Comment on the morphology of the erythrocytes.
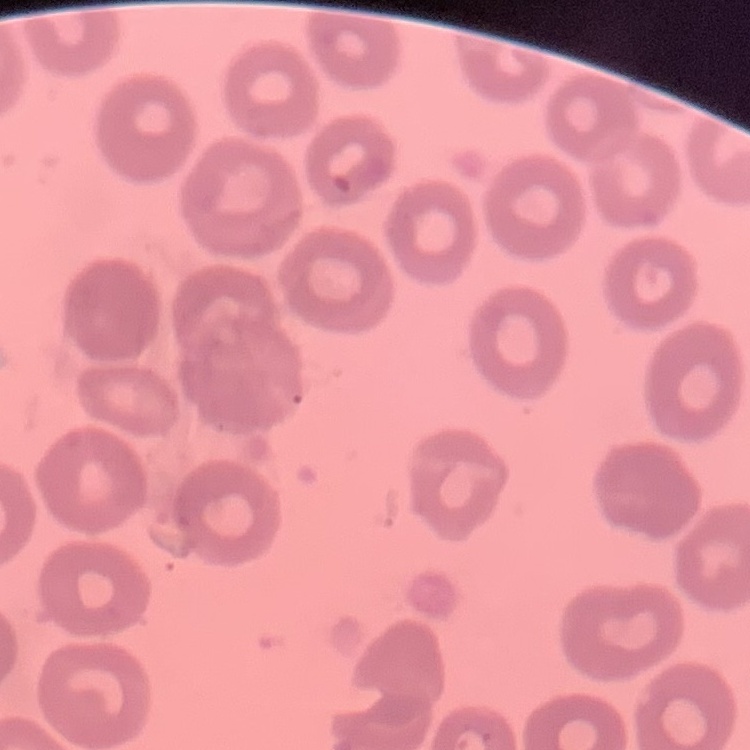

They show no rouleaux formation.

Summary:
  - Image type: one tile cut from a larger photomicrograph
  - Stain: Field's or Giemsa
  - Preparation: thin blood smear